Assess this cell for malaria.
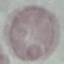

Uninfected.

stain: Giemsa
image_type: automatically extracted cell patch, resized to 64 × 64 pixels
preparation: thin blood smear
capture: smartphone camera at the microscope eyepiece